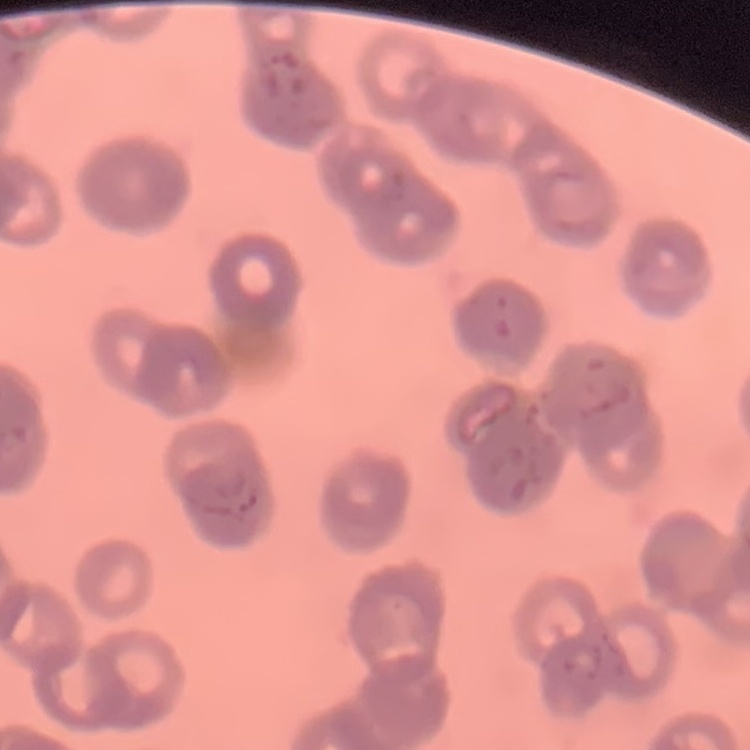

The erythrocytes exhibit rouleaux formation. Stained with either Field's or Giemsa. Thin blood smear. Square crop of a larger photomicrograph.